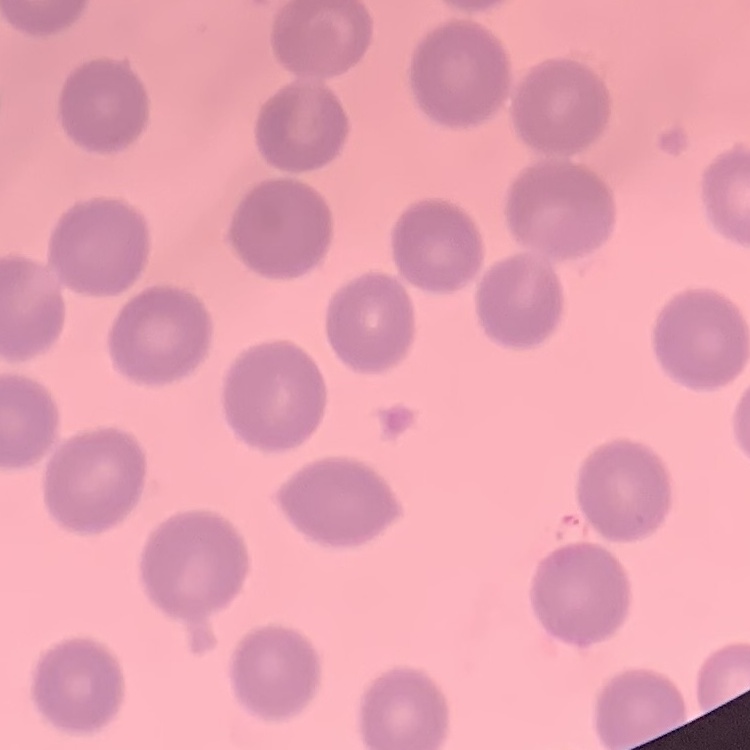
Summary:
  - Erythrocyte morphology: no rouleaux formation
  - Stain: Field's or Giemsa
  - Preparation: thin peripheral smear
  - Image type: one tile cut from a larger photomicrograph